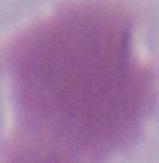 Micrograph. A red blood cell is shown. Captured at 1000x magnification.